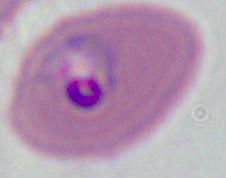

Captured at either 400x or 1000x magnification. A Plasmodium parasite is shown. Photomicrograph.